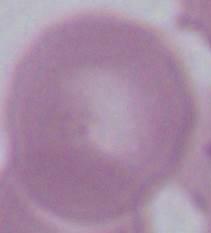
An erythrocyte is seen. Photomicrograph. 1000x magnification.